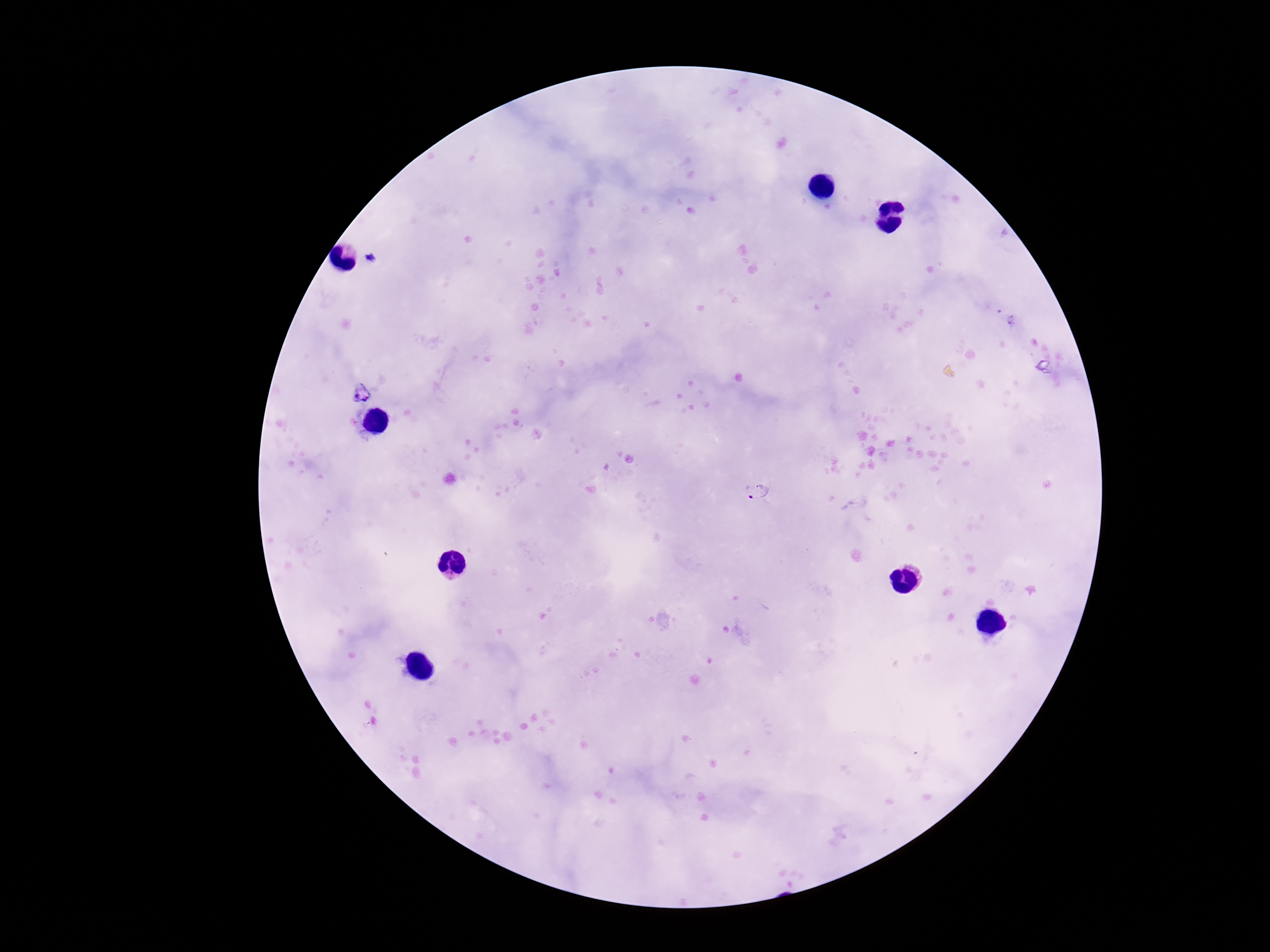

preparation = thick blood smear
magnification = 100x
stain = Giemsa
Plasmodium parasite locations = approximate centers as [x, y] in pixels: [371, 258], [758, 491]
field of view = one from this slide
patient malaria status = positive
capture = smartphone camera through the microscope eyepiece
image size = 1270×952 pixels